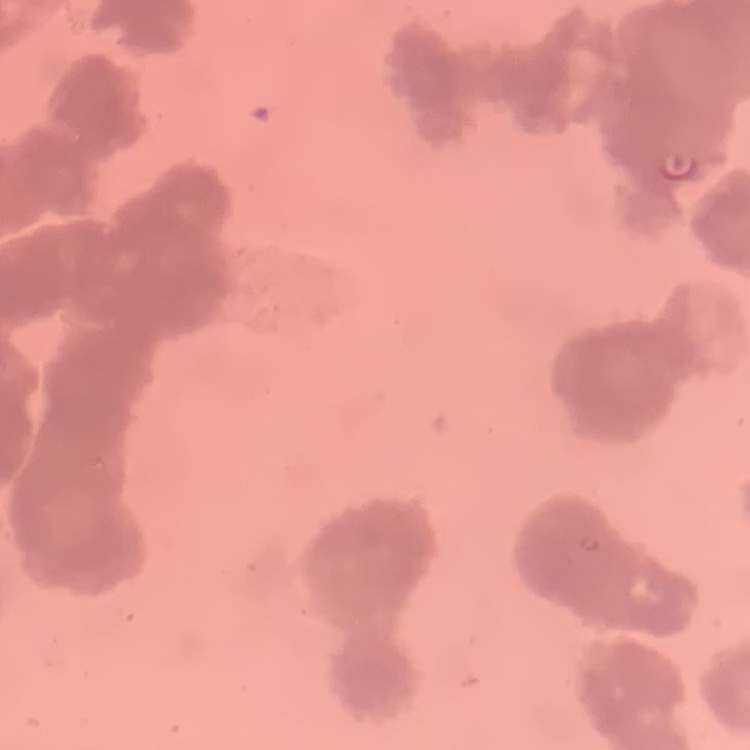

{
  "red_blood_cell_morphology": "rouleaux formation",
  "stain": "Field's or Giemsa",
  "image_type": "one tile cut from a larger photomicrograph",
  "preparation": "thin blood film"
}